Assess the morphology of the red blood cells.
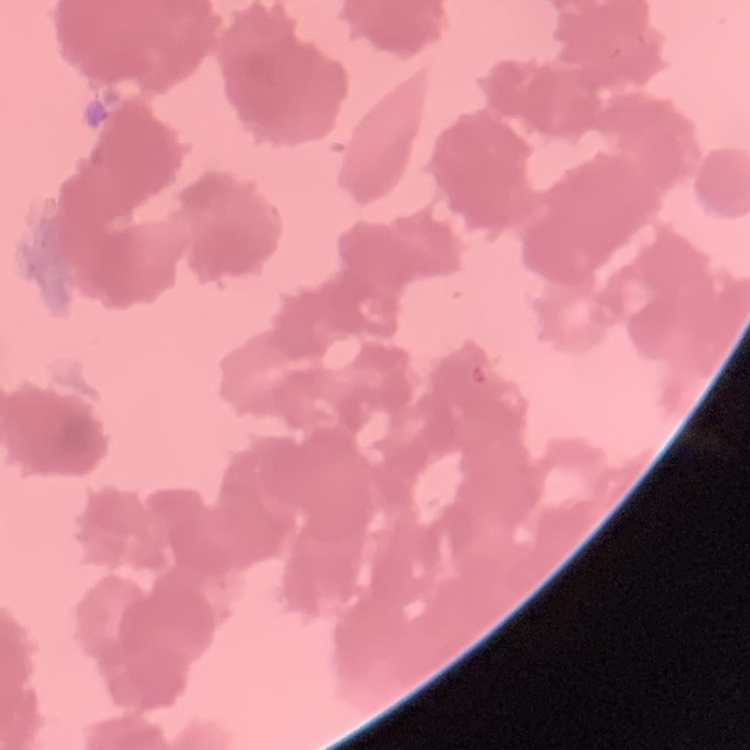

Rouleaux formation.

image_type: one tile cut from a larger photomicrograph
preparation: thin blood smear
stain: Field's or Giemsa